Locate every Plasmodium parasite.
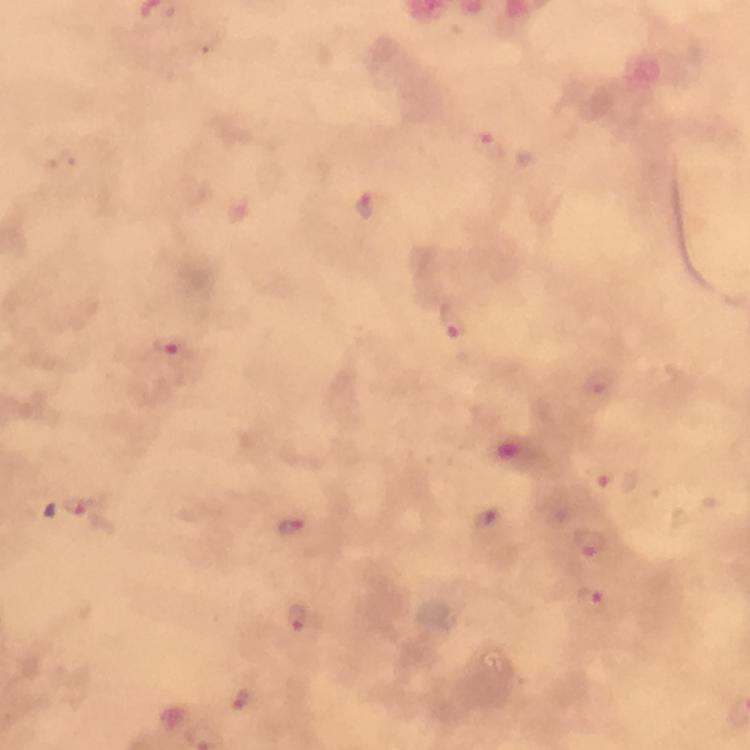

Approximate object centers, in pixels from the top-left corner.
Plasmodium parasites: (x=487, y=142), (x=367, y=203), (x=452, y=322), (x=171, y=345), (x=598, y=381), (x=604, y=477), (x=80, y=506), (x=292, y=527), (x=591, y=544), (x=592, y=602), (x=299, y=619), (x=240, y=700).

{
  "context": "from a malaria diagnostic workup",
  "capture": "smartphone camera through the microscope",
  "image_size": "750×750 pixels",
  "magnification": "100x",
  "immersion_oil": "used",
  "cropped_from": "a single field of view",
  "preparation": "thick blood smear",
  "stain": "Giemsa"
}